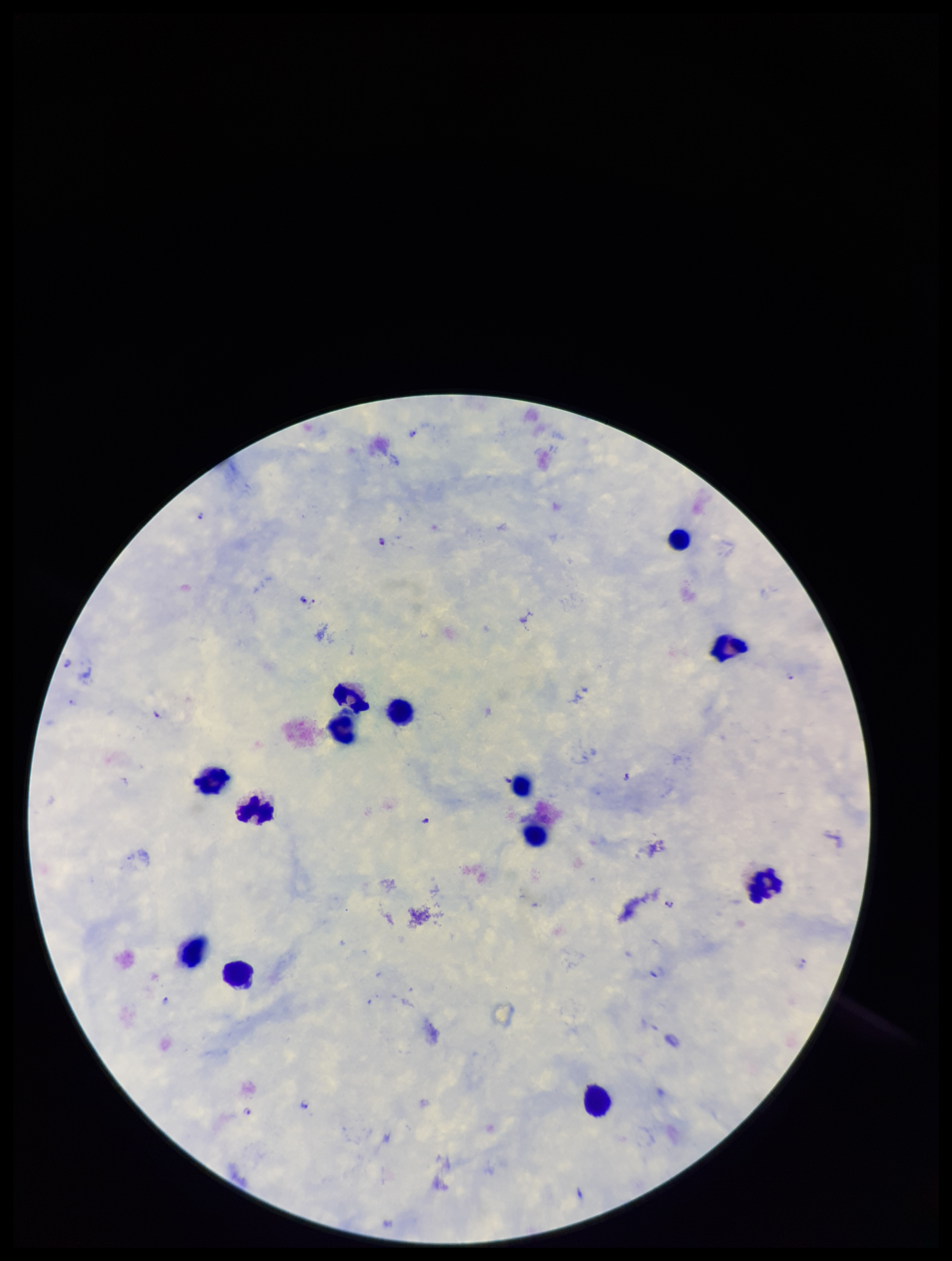

preparation = thick
species reported for this patient = Plasmodium falciparum
field of view = one from this slide
parasite count = 10
Plasmodium parasites = seen
image size = 952×1261 pixels
capture = smartphone photograph through the microscope eyepiece
patient malaria status = positive
leukocyte count = 13
stain = Giemsa